Outline each blood parasite and name the species.
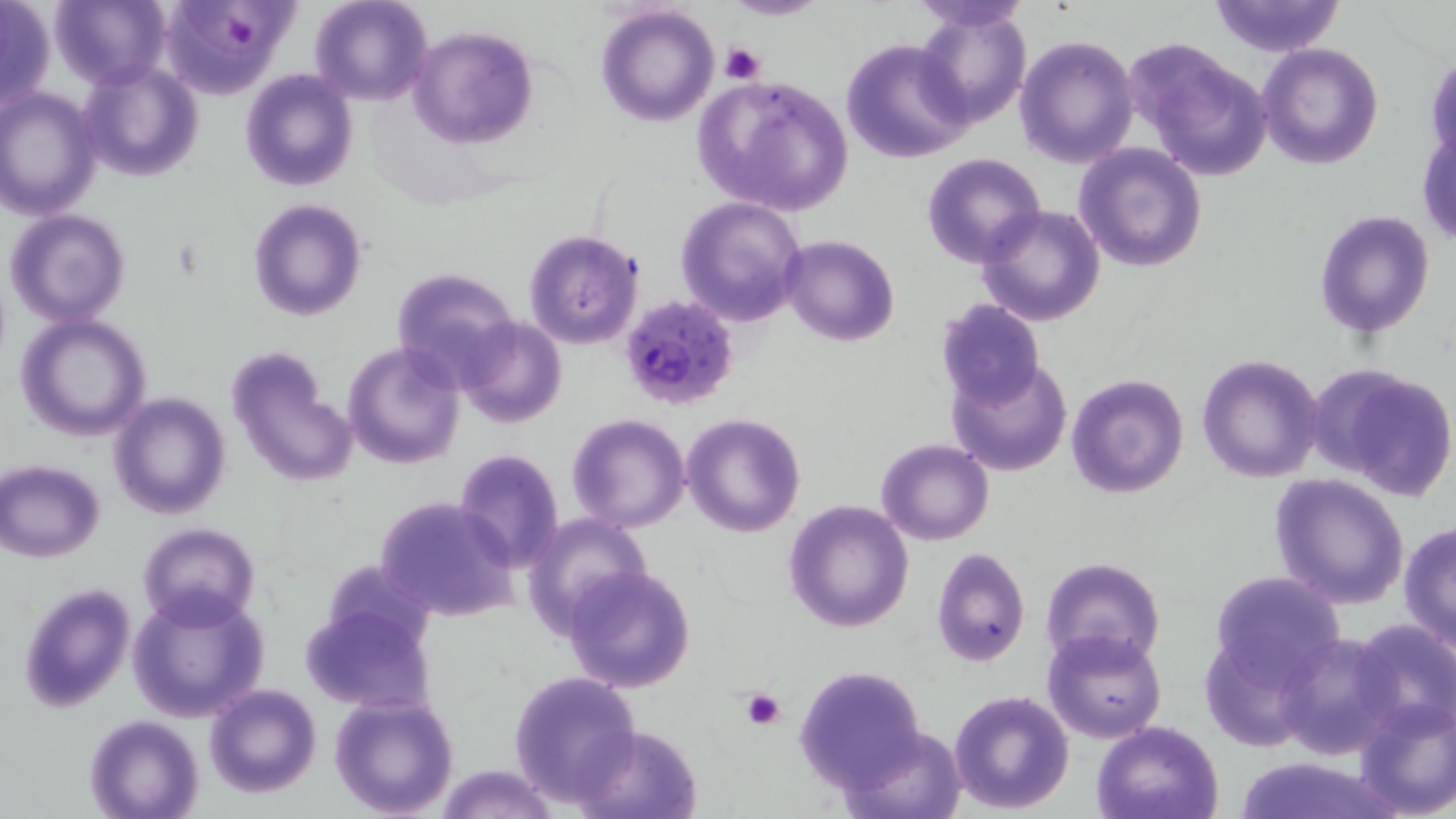
Approximate bounding boxes as named x1/y1/x2/y2 corners in pixels.
Plasmodium falciparum-infected red blood cells: (x1=620, y1=294, x2=737, y2=410).
No Plasmodium ovale, Plasmodium malariae, Plasmodium vivax, Babesia divergens, or Trypanosoma brucei observed.

Platelet locations: (x1=221, y1=13, x2=253, y2=46), (x1=720, y1=41, x2=766, y2=85), (x1=738, y1=688, x2=787, y2=731). Uninfected red blood cell locations: (x1=310, y1=0, x2=433, y2=106), (x1=724, y1=0, x2=826, y2=21), (x1=1208, y1=0, x2=1346, y2=55), (x1=0, y1=1, x2=54, y2=112), (x1=49, y1=1, x2=172, y2=87), (x1=156, y1=1, x2=298, y2=98), (x1=906, y1=1, x2=1036, y2=31), (x1=595, y1=4, x2=720, y2=128), (x1=914, y1=6, x2=1031, y2=128), (x1=409, y1=24, x2=538, y2=149), (x1=1014, y1=35, x2=1139, y2=169), (x1=841, y1=40, x2=973, y2=163), (x1=1128, y1=41, x2=1274, y2=179), (x1=1257, y1=43, x2=1383, y2=169), (x1=1426, y1=54, x2=1456, y2=168), (x1=79, y1=62, x2=204, y2=183), (x1=240, y1=68, x2=358, y2=191), (x1=698, y1=75, x2=852, y2=214), (x1=0, y1=88, x2=102, y2=219), (x1=1419, y1=117, x2=1455, y2=250), (x1=1073, y1=142, x2=1206, y2=272), (x1=921, y1=152, x2=1046, y2=268), (x1=675, y1=197, x2=807, y2=326), (x1=248, y1=199, x2=367, y2=321), (x1=977, y1=205, x2=1105, y2=326), (x1=5, y1=209, x2=131, y2=328), (x1=1312, y1=210, x2=1434, y2=337), (x1=523, y1=229, x2=646, y2=349), (x1=780, y1=234, x2=899, y2=347), (x1=389, y1=268, x2=520, y2=387), (x1=934, y1=298, x2=1046, y2=409), (x1=14, y1=313, x2=153, y2=441), (x1=457, y1=317, x2=567, y2=427), (x1=341, y1=342, x2=466, y2=469), (x1=224, y1=346, x2=359, y2=490), (x1=1197, y1=352, x2=1325, y2=484), (x1=946, y1=355, x2=1074, y2=477), (x1=1314, y1=364, x2=1456, y2=499), (x1=1065, y1=372, x2=1189, y2=499), (x1=108, y1=392, x2=231, y2=519), (x1=682, y1=413, x2=805, y2=537), (x1=567, y1=414, x2=690, y2=533), (x1=876, y1=438, x2=994, y2=545), (x1=451, y1=448, x2=565, y2=572), (x1=1, y1=459, x2=107, y2=561), (x1=1269, y1=473, x2=1409, y2=610), (x1=374, y1=495, x2=518, y2=623), (x1=782, y1=498, x2=914, y2=632), (x1=524, y1=512, x2=654, y2=636), (x1=137, y1=521, x2=259, y2=625), (x1=1398, y1=521, x2=1456, y2=657), (x1=931, y1=547, x2=1031, y2=667), (x1=1039, y1=557, x2=1166, y2=671), (x1=322, y1=560, x2=435, y2=655), (x1=559, y1=564, x2=698, y2=695), (x1=1209, y1=572, x2=1345, y2=688), (x1=16, y1=580, x2=137, y2=713), (x1=125, y1=589, x2=269, y2=724), (x1=298, y1=603, x2=436, y2=711), (x1=1348, y1=617, x2=1456, y2=736), (x1=1043, y1=627, x2=1166, y2=744), (x1=1200, y1=632, x2=1319, y2=751), (x1=1275, y1=632, x2=1401, y2=758), (x1=792, y1=664, x2=932, y2=790), (x1=507, y1=670, x2=642, y2=807), (x1=204, y1=683, x2=323, y2=800), (x1=948, y1=689, x2=1075, y2=812), (x1=328, y1=692, x2=460, y2=819), (x1=1352, y1=697, x2=1456, y2=818), (x1=84, y1=715, x2=203, y2=819), (x1=1092, y1=720, x2=1224, y2=819), (x1=574, y1=723, x2=701, y2=819), (x1=836, y1=724, x2=969, y2=817), (x1=1233, y1=753, x2=1399, y2=819), (x1=435, y1=762, x2=558, y2=819). Slide-level diagnosis: Plasmodium falciparum. Optical microscopy. Captured at 1000x magnification. Image is 1456×819 pixels. May-Grünwald-Giemsa-stained preparation. Thin blood smear. One field of a larger specimen.